Identify the parasite.
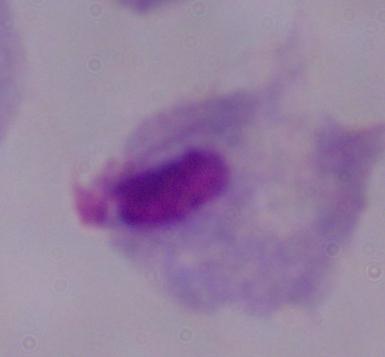

This is a trichomonad.

Summary:
  - Modality: photomicrograph
  - Magnification: 1000x